Give the preparation type.
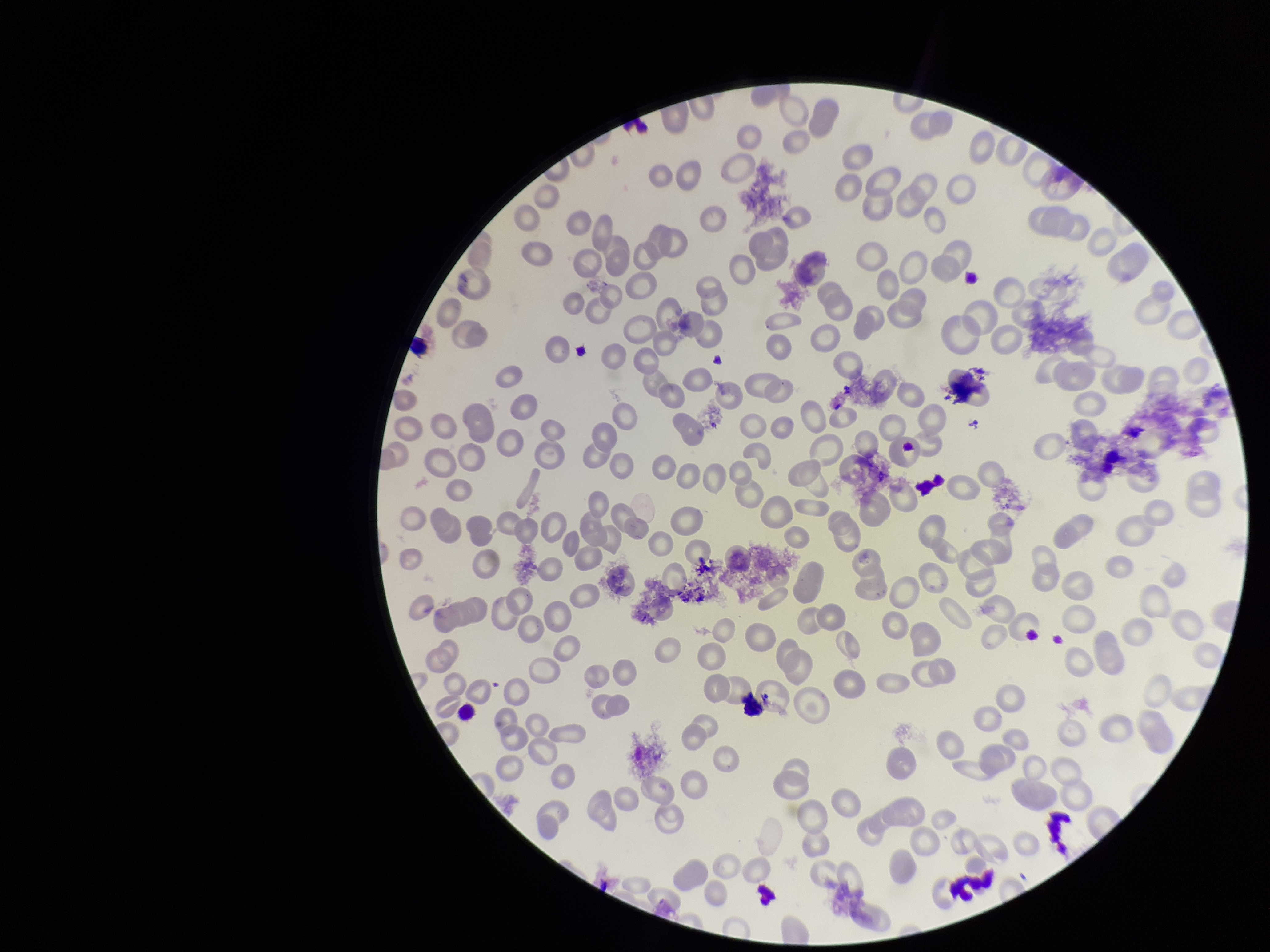

Thin.

image_size: 1270×952 pixels
stain: Giemsa
patient_malaria_status: negative
parasitized_red_blood_cell_count: 0
red_blood_cell_count: 194
field_of_view: single
parasitized_red_blood_cells: none identified
capture: smartphone photograph through the microscope eyepiece